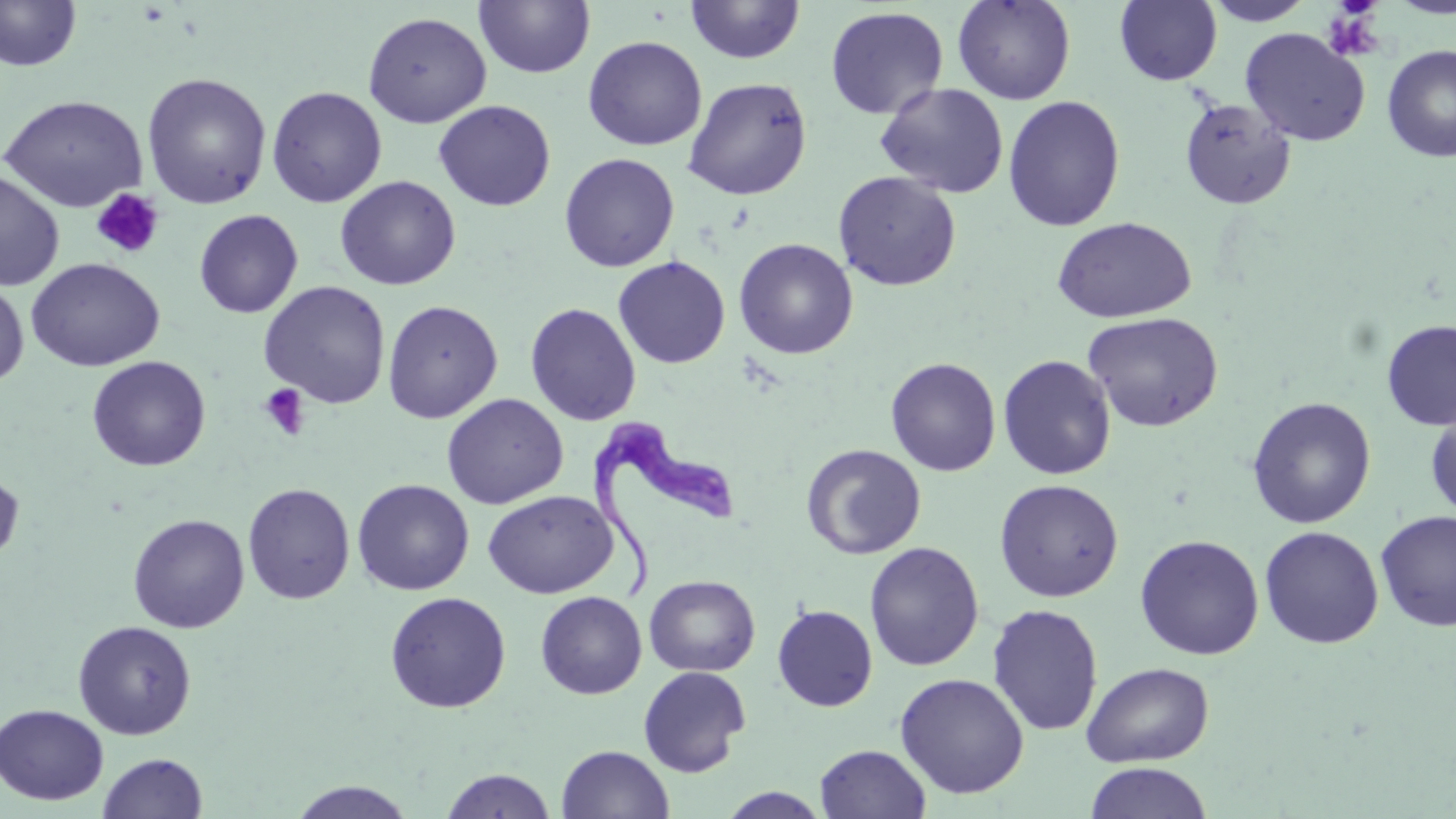

Approximate bounding boxes as named x1/y1/x2/y2 corners in pixels. Platelet locations: (x1=1322, y1=5, x2=1386, y2=63), (x1=91, y1=189, x2=164, y2=260), (x1=259, y1=383, x2=310, y2=440). Trypanosoma brucei locations: (x1=591, y1=412, x2=739, y2=601). Uninfected red blood cell locations: (x1=0, y1=0, x2=82, y2=72), (x1=952, y1=0, x2=1076, y2=105), (x1=1114, y1=0, x2=1222, y2=85), (x1=1203, y1=0, x2=1316, y2=26), (x1=1390, y1=0, x2=1456, y2=18), (x1=474, y1=1, x2=596, y2=79), (x1=685, y1=1, x2=806, y2=64), (x1=825, y1=6, x2=948, y2=119), (x1=362, y1=11, x2=491, y2=128), (x1=1240, y1=27, x2=1370, y2=146), (x1=582, y1=35, x2=707, y2=151), (x1=1382, y1=45, x2=1456, y2=162), (x1=141, y1=72, x2=272, y2=209), (x1=683, y1=77, x2=812, y2=200), (x1=875, y1=82, x2=1010, y2=198), (x1=266, y1=86, x2=387, y2=207), (x1=1, y1=94, x2=148, y2=212), (x1=1002, y1=95, x2=1126, y2=232), (x1=1178, y1=97, x2=1296, y2=210), (x1=434, y1=100, x2=556, y2=211), (x1=559, y1=152, x2=679, y2=272), (x1=0, y1=170, x2=65, y2=291), (x1=833, y1=171, x2=962, y2=291), (x1=335, y1=175, x2=461, y2=290), (x1=194, y1=209, x2=303, y2=318), (x1=1051, y1=216, x2=1197, y2=324), (x1=734, y1=238, x2=858, y2=359), (x1=612, y1=256, x2=731, y2=369), (x1=26, y1=258, x2=164, y2=372), (x1=0, y1=279, x2=29, y2=388), (x1=258, y1=280, x2=391, y2=409), (x1=382, y1=299, x2=503, y2=424), (x1=525, y1=302, x2=642, y2=426), (x1=1082, y1=311, x2=1224, y2=432), (x1=1381, y1=320, x2=1456, y2=429), (x1=997, y1=354, x2=1117, y2=480), (x1=87, y1=356, x2=210, y2=471), (x1=885, y1=357, x2=1001, y2=476), (x1=442, y1=393, x2=568, y2=509), (x1=1246, y1=396, x2=1377, y2=528), (x1=1425, y1=402, x2=1456, y2=522), (x1=801, y1=443, x2=926, y2=560), (x1=0, y1=468, x2=24, y2=567), (x1=993, y1=478, x2=1124, y2=602), (x1=352, y1=479, x2=474, y2=595), (x1=242, y1=482, x2=355, y2=604), (x1=482, y1=490, x2=618, y2=599), (x1=1375, y1=509, x2=1456, y2=632), (x1=128, y1=514, x2=249, y2=633), (x1=1259, y1=525, x2=1384, y2=649), (x1=1135, y1=534, x2=1264, y2=660), (x1=864, y1=542, x2=984, y2=671), (x1=644, y1=575, x2=760, y2=677), (x1=385, y1=591, x2=511, y2=713), (x1=535, y1=591, x2=647, y2=699), (x1=987, y1=603, x2=1103, y2=736), (x1=772, y1=604, x2=878, y2=711), (x1=72, y1=621, x2=197, y2=740), (x1=1081, y1=661, x2=1214, y2=767), (x1=638, y1=666, x2=751, y2=777), (x1=895, y1=672, x2=1030, y2=799), (x1=0, y1=704, x2=109, y2=805), (x1=815, y1=744, x2=931, y2=818), (x1=557, y1=745, x2=675, y2=819), (x1=98, y1=752, x2=208, y2=818), (x1=1084, y1=762, x2=1214, y2=819), (x1=440, y1=769, x2=556, y2=818), (x1=287, y1=781, x2=416, y2=818), (x1=716, y1=787, x2=834, y2=818). Slide-level diagnosis: Trypanosoma brucei. Captured at 1000x magnification. Light microscopy. May-Grünwald-Giemsa-stained preparation. Image is 1456×819 pixels. Thin blood film. One field of a larger specimen.